State which parasite is depicted.
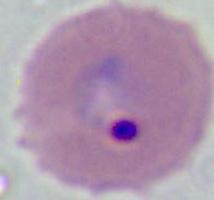
Plasmodium.

400x or 1000x magnification. Micrograph.